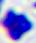
magnification: 400x
modality: photomicrograph
identification: white blood cell